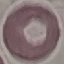
Malaria status: uninfected. Photographed with a smartphone camera at the microscope eyepiece. Thin blood smear. Giemsa-stained preparation. Automatically extracted cell patch, resized to 64 × 64 pixels.